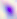
Summary:
  - Magnification: 400x
  - Identification: Toxoplasma gondii
  - Modality: micrograph